Give the extent of all Plasmodium falciparum-infected red blood cells.
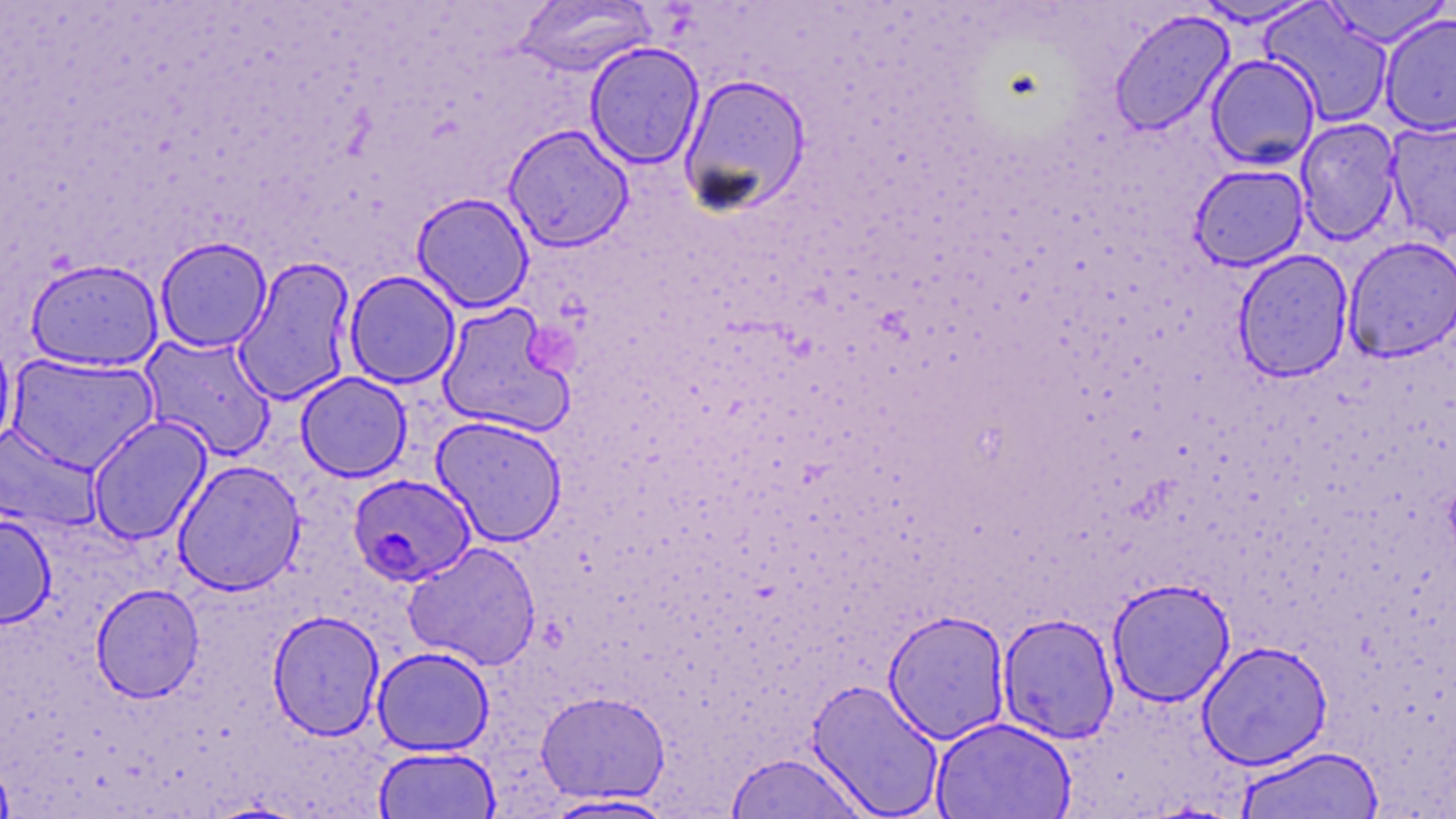
Approximate bounding boxes as named x1/y1/x2/y2 corners in pixels.
Plasmodium falciparum-infected red blood cells: (x1=347, y1=474, x2=480, y2=588).

Platelet locations: (x1=527, y1=326, x2=580, y2=376). Uninfected red blood cell locations: (x1=1189, y1=0, x2=1326, y2=28), (x1=1320, y1=0, x2=1452, y2=48), (x1=512, y1=1, x2=657, y2=77), (x1=1260, y1=3, x2=1394, y2=127), (x1=1108, y1=8, x2=1235, y2=137), (x1=1378, y1=12, x2=1456, y2=136), (x1=585, y1=42, x2=705, y2=169), (x1=1206, y1=53, x2=1321, y2=170), (x1=678, y1=72, x2=812, y2=216), (x1=1295, y1=118, x2=1402, y2=244), (x1=1384, y1=118, x2=1456, y2=243), (x1=502, y1=123, x2=634, y2=253), (x1=1189, y1=164, x2=1309, y2=271), (x1=411, y1=192, x2=534, y2=312), (x1=155, y1=236, x2=273, y2=353), (x1=1343, y1=236, x2=1456, y2=362), (x1=1232, y1=249, x2=1354, y2=382), (x1=232, y1=256, x2=357, y2=405), (x1=25, y1=257, x2=163, y2=372), (x1=343, y1=270, x2=461, y2=388), (x1=436, y1=302, x2=576, y2=437), (x1=0, y1=328, x2=17, y2=457), (x1=138, y1=332, x2=276, y2=461), (x1=6, y1=353, x2=159, y2=473), (x1=296, y1=371, x2=412, y2=481), (x1=86, y1=415, x2=212, y2=545), (x1=431, y1=415, x2=567, y2=545), (x1=0, y1=422, x2=103, y2=532), (x1=172, y1=459, x2=306, y2=595), (x1=0, y1=514, x2=56, y2=628), (x1=403, y1=542, x2=541, y2=670), (x1=1106, y1=577, x2=1236, y2=707), (x1=91, y1=583, x2=204, y2=703), (x1=267, y1=610, x2=385, y2=741), (x1=883, y1=610, x2=1011, y2=744), (x1=998, y1=612, x2=1120, y2=743), (x1=1197, y1=640, x2=1333, y2=771), (x1=371, y1=646, x2=494, y2=756), (x1=806, y1=677, x2=945, y2=818), (x1=536, y1=691, x2=670, y2=803), (x1=931, y1=716, x2=1077, y2=819), (x1=1235, y1=744, x2=1385, y2=818), (x1=373, y1=745, x2=501, y2=818), (x1=726, y1=752, x2=870, y2=819), (x1=0, y1=756, x2=14, y2=817), (x1=540, y1=793, x2=681, y2=817). Slide-level diagnosis: Plasmodium falciparum. Image is 1456×819 pixels. Captured at 1000x magnification. Optical microscopy. May-Grünwald-Giemsa-stained preparation. Thin blood smear. One field of a larger specimen.